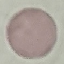
malaria status = uninfected
stain = Giemsa
image type = cell patch, automatically extracted from a larger field of view and resized to 64 × 64 pixels
preparation = thin blood smear
capture = smartphone camera at the microscope eyepiece